Classify this cell by malaria status.
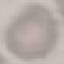
Uninfected.

Automatically extracted cell patch, resized to 64 × 64 pixels. Thin smear of blood. Photographed with a smartphone camera at the microscope eyepiece. Giemsa-stained preparation.